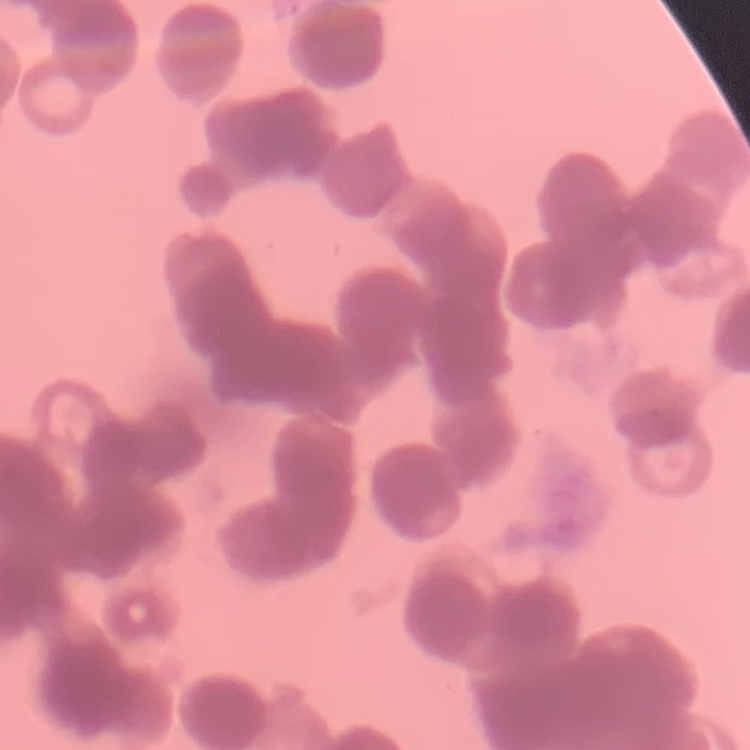

Summary:
  - Red blood cell morphology: rouleaux formation
  - Image type: one tile cut from a larger photomicrograph
  - Stain: Field's or Giemsa
  - Preparation: thin blood smear